Give the extent of all Plasmodium falciparum-infected red blood cells.
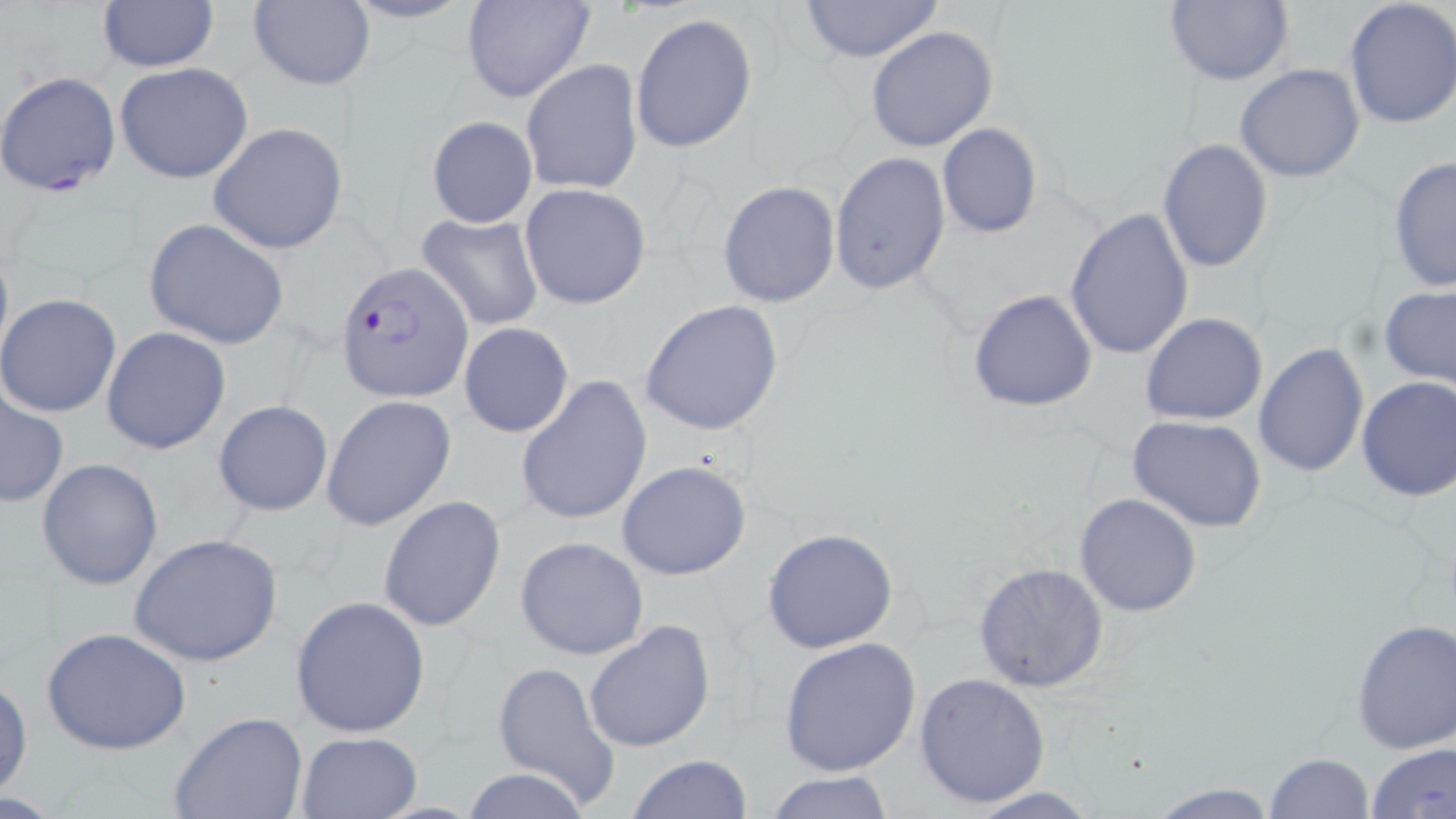
Approximate bounding boxes as (x1,y1)-(x2,y2) corner pairs in pixels.
Plasmodium falciparum-infected red blood cells: (1,70)-(122,198), (338,261)-(471,403).

slide-level diagnosis = Plasmodium falciparum
preparation = thin blood film
magnification = 1000x
image size = 1456×819 pixels
stain = May-Grünwald-Giemsa
uninfected red blood cell locations = approximate bounding boxes as (x1,y1)-(x2,y2) corner pairs in pixels: (339,0)-(479,26), (795,0)-(945,63), (1164,0)-(1294,87), (1342,0)-(1456,130), (97,1)-(217,72), (247,1)-(374,90), (460,1)-(595,104), (630,13)-(758,152), (867,25)-(999,152), (522,59)-(641,195), (114,62)-(254,185), (1235,63)-(1365,184), (426,115)-(537,229), (208,122)-(349,254), (937,123)-(1043,238), (1156,139)-(1274,272), (829,151)-(950,295), (1386,155)-(1456,293), (718,180)-(840,307), (519,183)-(652,309), (1063,206)-(1195,362), (417,213)-(544,331), (144,219)-(289,350), (0,236)-(13,369), (1379,286)-(1456,388), (968,289)-(1098,412), (0,293)-(121,418), (640,299)-(786,436), (1140,312)-(1268,425), (458,322)-(574,438), (102,327)-(231,456), (1250,341)-(1367,477), (1355,374)-(1456,501), (514,375)-(652,525), (2,385)-(69,508), (322,395)-(456,531), (213,398)-(334,516), (1127,416)-(1268,533), (37,459)-(165,591), (616,460)-(752,580), (1074,493)-(1203,617), (377,494)-(507,633), (761,527)-(898,653), (129,532)-(285,668), (515,536)-(651,660), (973,562)-(1110,692), (289,596)-(431,739), (1350,617)-(1456,754), (584,619)-(715,753), (41,626)-(191,756), (778,637)-(921,777), (491,660)-(619,809), (915,672)-(1051,809), (0,675)-(31,802), (170,713)-(307,819), (295,733)-(423,819), (1366,742)-(1456,818), (1264,753)-(1375,819), (625,754)-(755,818), (461,767)-(592,819), (763,770)-(895,819), (1142,781)-(1284,818), (962,786)-(1103,818)
modality = optical microscopy
field of view = single